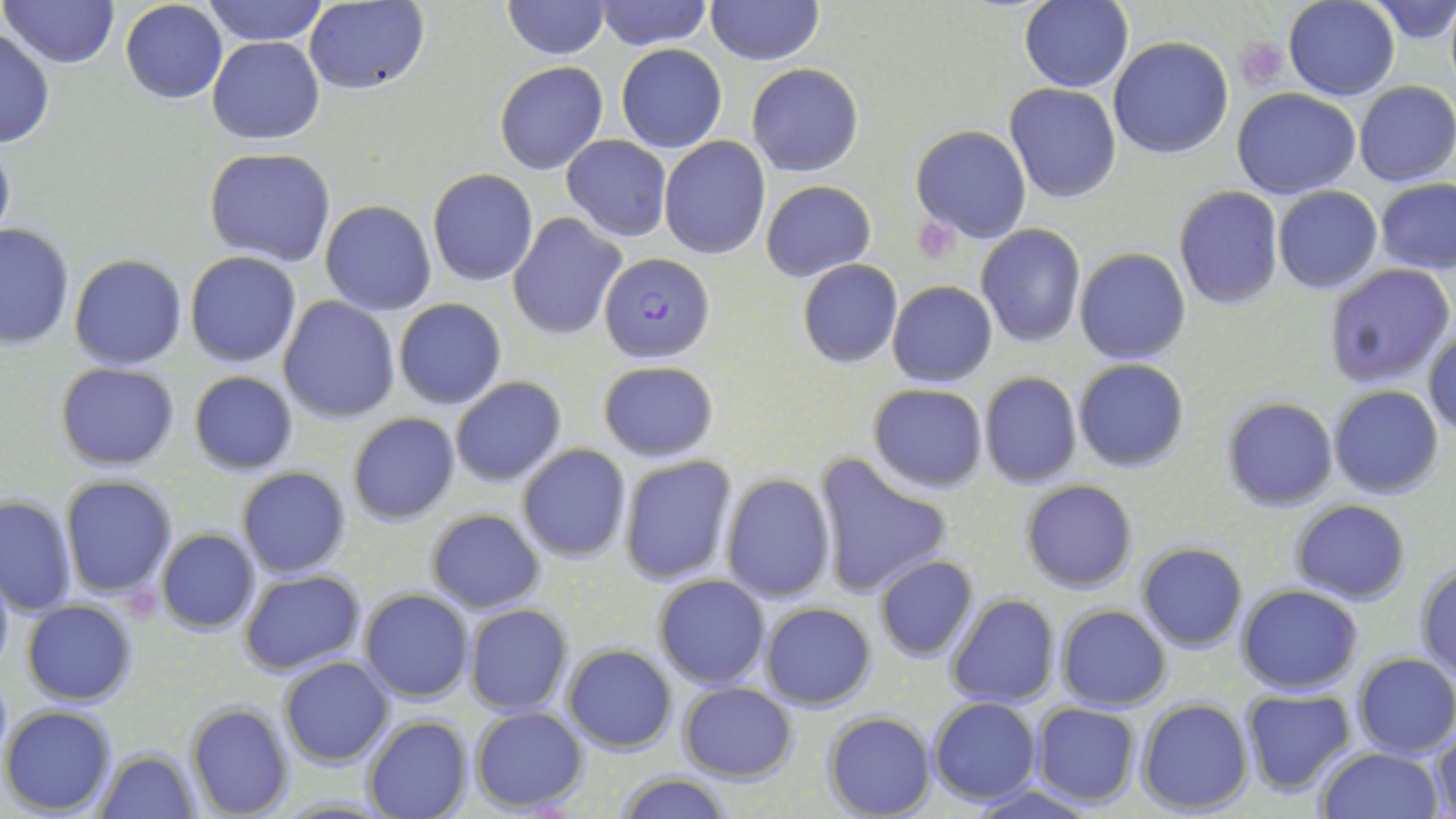

Summary:
  - Coordinate format: approximate bounding boxes as (x1,y1)-(x2,y2) corner pairs in pixels
  - Platelet locations: (1236,39)-(1289,88), (912,220)-(962,264)
  - Plasmodium falciparum-infected red blood cell locations: (600,250)-(714,363)
  - Uninfected red blood cell locations: (2,0)-(119,68), (202,0)-(328,46), (705,0)-(822,65), (1284,0)-(1399,100), (1372,0)-(1456,46), (302,1)-(429,95), (501,1)-(610,60), (592,1)-(711,50), (1020,1)-(1132,91), (119,2)-(228,104), (0,27)-(54,150), (207,35)-(325,145), (1108,36)-(1234,157), (616,43)-(727,153), (494,60)-(608,175), (746,62)-(864,177), (1355,80)-(1455,186), (1006,83)-(1121,203), (1233,88)-(1361,200), (910,124)-(1032,244), (0,131)-(14,248), (560,135)-(669,239), (660,137)-(769,258), (204,147)-(336,267), (427,168)-(538,287), (1375,179)-(1456,273), (762,180)-(875,280), (1173,186)-(1284,310), (1273,186)-(1382,293), (320,200)-(436,316), (508,212)-(626,341), (0,222)-(76,350), (975,226)-(1086,347), (1076,248)-(1191,365), (183,251)-(302,367), (68,254)-(189,370), (797,259)-(903,369), (1322,263)-(1452,389), (887,281)-(996,386), (277,297)-(400,423), (393,298)-(506,409), (1424,325)-(1456,438), (1073,359)-(1190,473), (598,360)-(719,463), (55,362)-(181,471), (188,371)-(298,476), (979,372)-(1082,488), (449,377)-(566,486), (867,384)-(989,493), (1330,386)-(1444,499), (1223,397)-(1339,513), (347,413)-(461,525), (517,444)-(632,563), (618,454)-(739,586), (811,454)-(954,597), (237,467)-(351,578), (719,473)-(835,603), (60,475)-(178,598), (1021,480)-(1138,592), (0,494)-(76,618), (1290,499)-(1411,603), (425,508)-(545,613), (154,528)-(260,635), (1136,542)-(1248,652), (873,555)-(979,663), (1415,559)-(1456,680), (0,561)-(14,678), (239,569)-(367,676), (652,573)-(771,690), (1236,584)-(1365,695), (359,588)-(475,705), (946,594)-(1060,708), (21,599)-(139,706), (760,603)-(877,710), (463,604)-(573,716), (1055,605)-(1172,711), (562,643)-(677,755), (1351,651)-(1456,759), (279,656)-(393,768), (678,682)-(797,781), (1238,687)-(1357,794), (928,698)-(1042,806), (1137,698)-(1252,815), (185,702)-(294,817), (1031,702)-(1140,806), (1,705)-(118,816), (469,707)-(589,812), (823,710)-(936,818), (362,716)-(471,819), (1430,722)-(1456,819), (95,748)-(200,819), (1314,748)-(1444,819), (613,771)-(732,819), (964,784)-(1106,819)
  - Slide-level diagnosis: Plasmodium falciparum
  - Magnification: 1000x
  - Field of view: one of a larger specimen
  - Image size: 1456×819 pixels
  - Stain: May-Grünwald-Giemsa
  - Preparation: thin blood smear
  - Modality: optical microscopy